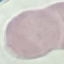 Malaria status: uninfected. Cell patch, automatically extracted from a larger field of view and resized to 64 × 64 pixels. Thin blood film. Acquired by smartphone through the microscope eyepiece. Giemsa-stained preparation.